Identify the cell.
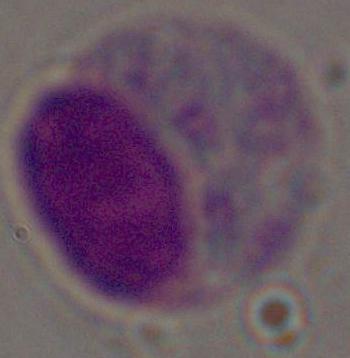

A leukocyte.

modality: photomicrograph
magnification: 1000x